Locate and identify every blood parasite.
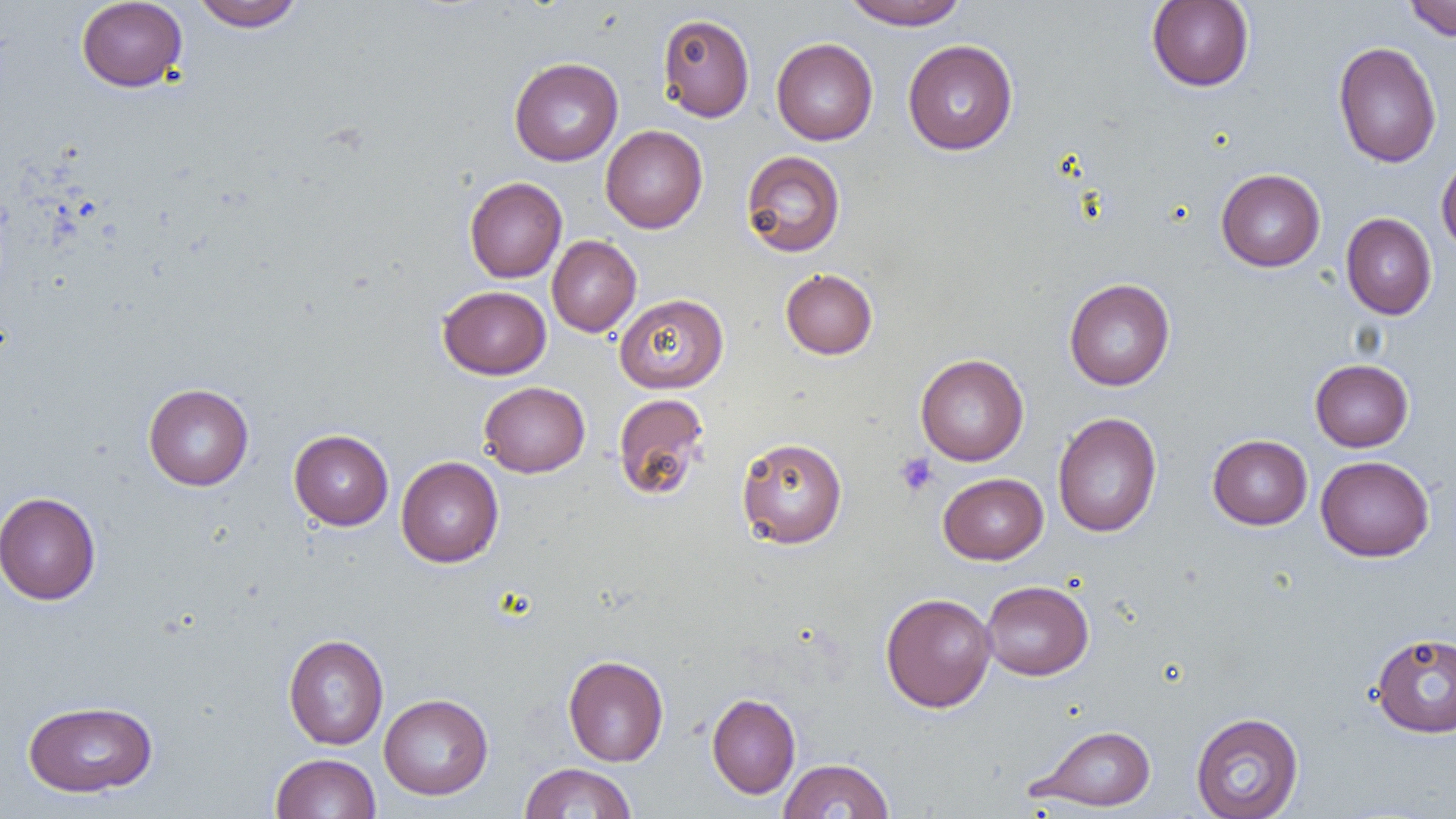

No blood parasites seen.

Approximate bounding boxes as (x1, y1, x2, y2) in pixels. Platelet locations: (894, 452, 937, 496). Uninfected red blood cell locations: (76, 0, 188, 92), (191, 0, 302, 31), (842, 0, 969, 30), (1404, 0, 1456, 41), (1146, 1, 1254, 91), (657, 13, 755, 122), (771, 38, 878, 145), (902, 39, 1018, 155), (1333, 41, 1442, 168), (509, 57, 623, 166), (600, 125, 707, 233), (741, 150, 846, 258), (1436, 155, 1456, 258), (1216, 169, 1325, 272), (464, 177, 567, 283), (1341, 213, 1437, 319), (547, 235, 642, 336), (780, 268, 878, 359), (1064, 278, 1175, 390), (438, 285, 551, 379), (614, 293, 729, 394), (915, 354, 1029, 466), (1310, 359, 1413, 452), (479, 382, 590, 477), (143, 383, 254, 491), (613, 393, 710, 501), (1052, 411, 1162, 538), (289, 429, 393, 530), (1207, 434, 1313, 530), (736, 437, 848, 549), (1315, 455, 1435, 562), (396, 456, 504, 567), (938, 472, 1048, 565), (0, 492, 101, 605), (981, 579, 1093, 680), (880, 592, 996, 713), (1370, 631, 1456, 738), (283, 634, 388, 750), (563, 655, 668, 766), (707, 692, 801, 799), (379, 694, 493, 800), (22, 699, 157, 797), (1191, 712, 1304, 818), (1030, 724, 1156, 811), (271, 753, 381, 819), (778, 758, 894, 818), (519, 762, 637, 818). Slide-level diagnosis: no evidence of blood parasites. 1000x magnification. One field of a larger specimen. Light microscopy. Image is 1456×819 pixels. Thin blood smear.